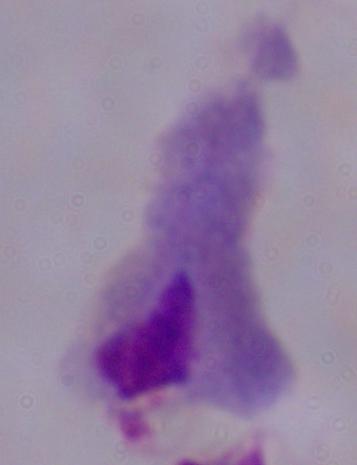
modality: photomicrograph
magnification: 1000x
identification: trichomonad